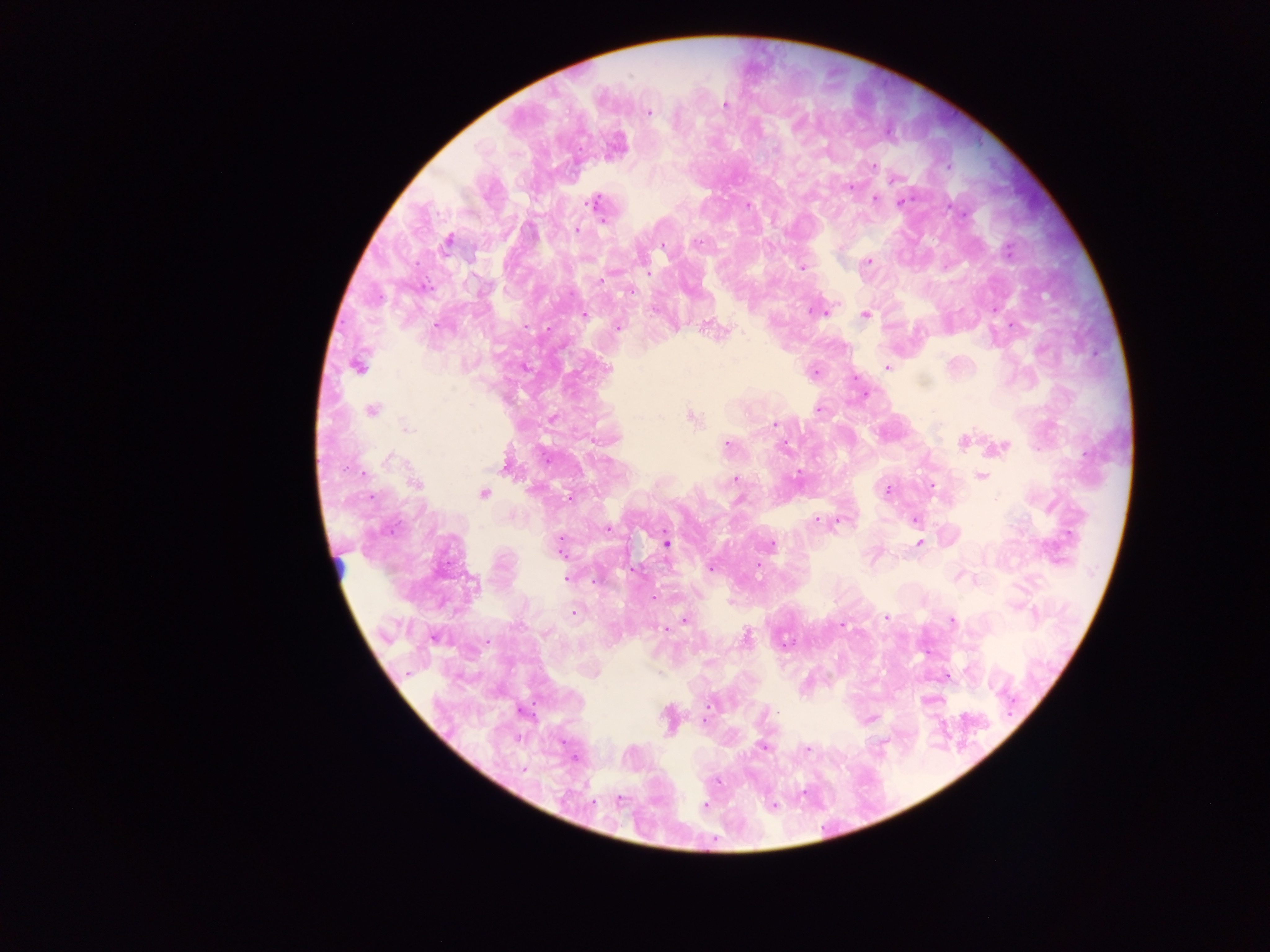
Approximate centers as x y in pixels. Leukocyte locations: 340 570. Plasmodium parasite locations: 725 104; 649 112; 775 150; 873 166; 948 167; 896 178; 851 188; 875 198; 902 201; 594 204; 748 205; 576 230; 448 241; 697 243; 664 246; 1008 250; 868 261; 802 267; 648 272; 601 280; 630 291; 655 310; 813 310; 865 314; 585 315; 437 326; 618 327; 358 366; 887 367; 608 368; 814 373; 819 409; 372 411; 691 418; 774 424; 408 428; 964 440; 727 445; 785 446; 1000 447; 390 459; 982 476; 735 479; 415 483; 931 487; 887 490; 484 493; 739 500; 915 520; 816 521; 608 530; 919 543; 667 544; 770 545; 560 548; 757 565; 711 569; 959 576; 566 578; 574 612; 885 618; 684 620; 952 621; 842 626; 666 629; 746 638; 710 705; 762 747; 807 748; 523 770; 620 801; 705 806; 773 806. Single field of view. Mobile-phone photograph taken through the microscope. Image is 1270×952 pixels. Sample from Ghana. Thick blood film.